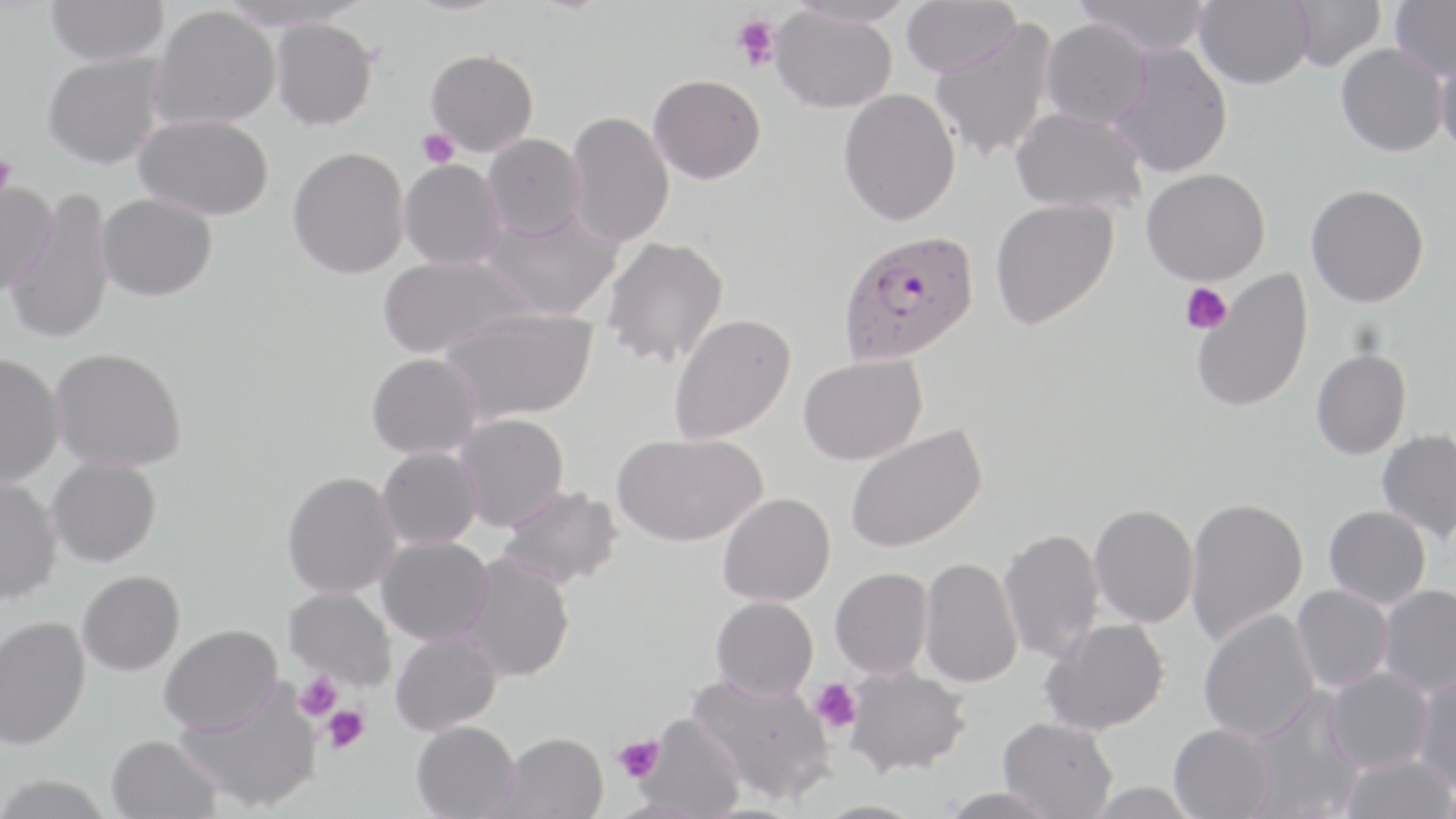 Approximate bounding boxes as (x1,y1)-(x2,y2) corner pairs in pixels. Plasmodium falciparum-infected red blood cell locations: (837,229)-(979,365). Uninfected red blood cell locations: (45,0)-(169,67), (216,0)-(371,32), (398,0)-(513,16), (785,0)-(916,29), (901,0)-(1021,77), (1075,0)-(1212,56), (1195,0)-(1313,89), (1288,0)-(1385,71), (1389,0)-(1456,80), (150,6)-(281,130), (770,6)-(897,113), (928,18)-(1058,163), (270,19)-(377,130), (1040,19)-(1152,129), (1107,43)-(1233,179), (1335,43)-(1448,157), (1435,45)-(1456,159), (426,49)-(538,156), (43,53)-(166,172), (648,73)-(767,184), (838,88)-(961,226), (1010,107)-(1146,213), (566,110)-(674,248), (133,114)-(274,221), (482,133)-(586,240), (288,146)-(410,279), (398,159)-(507,270), (1141,168)-(1270,286), (0,182)-(57,300), (1305,184)-(1429,307), (5,192)-(115,345), (96,192)-(217,302), (990,198)-(1119,331), (480,208)-(623,322), (601,236)-(729,368), (377,254)-(536,361), (1191,270)-(1314,415), (439,307)-(599,425), (668,313)-(797,444), (50,347)-(187,471), (1311,348)-(1411,460), (367,352)-(482,459), (0,353)-(65,488), (798,354)-(927,466), (454,413)-(569,532), (845,423)-(987,554), (1376,429)-(1456,541), (612,432)-(767,547), (376,447)-(482,549), (47,457)-(161,566), (282,470)-(402,598), (0,477)-(62,605), (499,485)-(624,591), (717,493)-(835,607), (1184,496)-(1308,646), (1088,503)-(1199,628), (1324,506)-(1431,609), (998,527)-(1104,664), (375,536)-(493,645), (459,553)-(575,682), (919,557)-(1023,687), (830,567)-(934,679), (77,570)-(184,676), (1291,585)-(1393,692), (1377,585)-(1456,698), (283,587)-(396,692), (711,596)-(818,700), (1198,608)-(1319,743), (0,616)-(90,751), (1041,618)-(1169,735), (158,624)-(283,736), (390,630)-(502,736), (845,665)-(970,776), (1325,667)-(1434,773), (686,673)-(837,804), (1412,673)-(1456,793), (174,682)-(321,813), (1244,691)-(1364,819), (637,714)-(746,819), (998,717)-(1117,818), (411,720)-(521,819), (1168,723)-(1276,819), (493,732)-(608,819), (106,734)-(221,819), (1338,753)-(1456,819), (0,774)-(113,819), (1083,782)-(1202,819), (937,787)-(1060,819), (809,800)-(928,819). Platelet locations: (731,14)-(780,72), (417,128)-(460,168), (0,154)-(18,197), (1180,282)-(1232,335), (293,670)-(342,721), (810,678)-(863,734), (321,705)-(370,754), (613,735)-(663,781). Slide-level diagnosis: Plasmodium falciparum. Optical microscopy. May-Grünwald-Giemsa stain. Thin blood film. 1000x magnification. Image is 1456×819 pixels. Single field of view.